Outline each Plasmodium ovale-infected red blood cell.
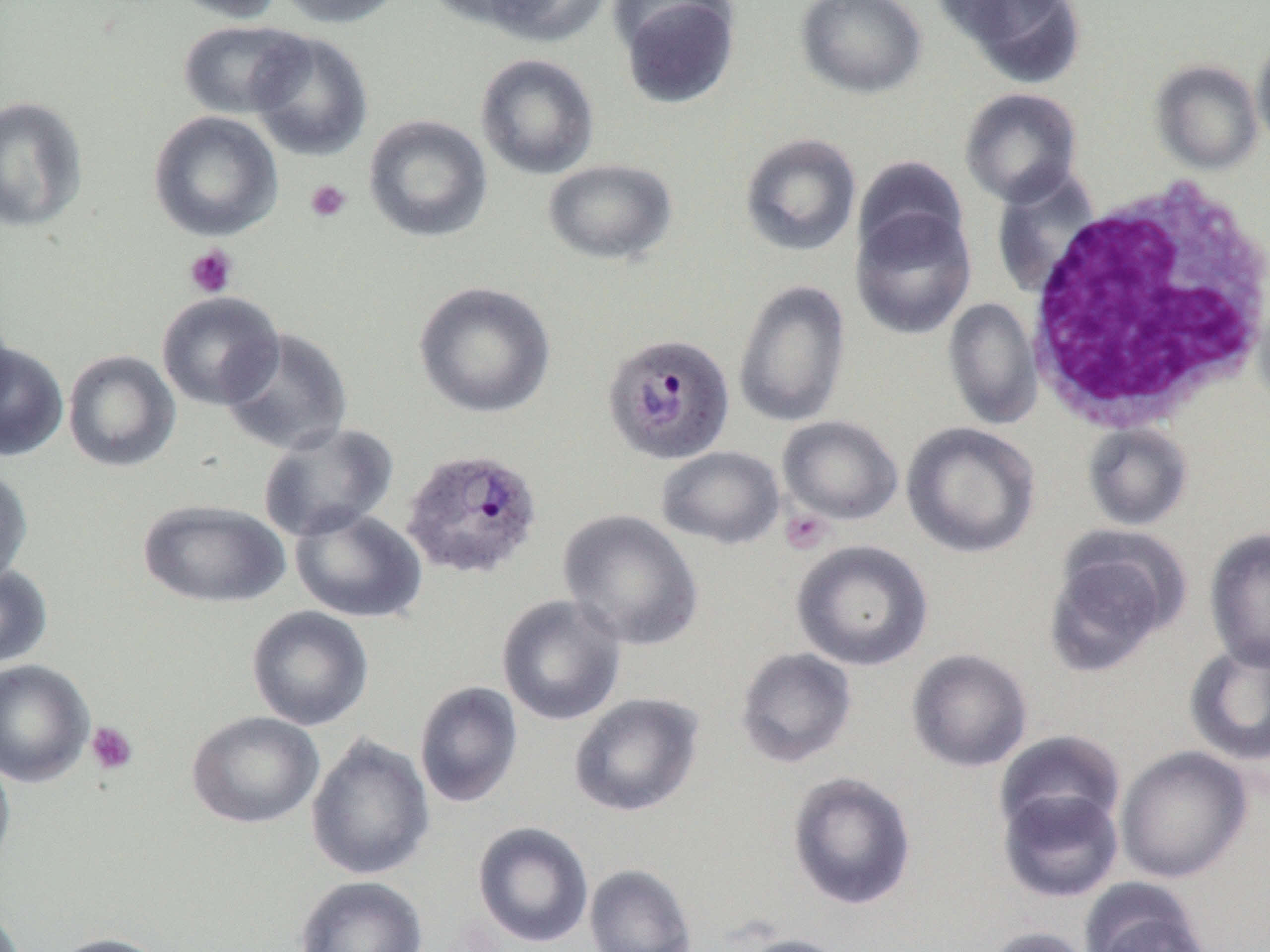
Approximate bounding boxes as (x1,y1)-(x2,y2) corner pairs in pixels.
Plasmodium ovale-infected red blood cells: (601,333)-(735,465), (401,447)-(543,581).

slide_level_diagnosis: Plasmodium ovale
magnification: 1000x
preparation: thin blood smear
field_of_view: one of a larger specimen
image_size: 1270×952 pixels
modality: light microscopy
uninfected_red_blood_cell_locations: 'approximate bounding boxes as (x1,y1)-(x2,y2) corner pairs in pixels: (165,0)-(284,23), (275,0)-(407,28), (421,0)-(556,32), (478,0)-(612,47), (611,0)-(741,109), (795,0)-(926,99), (929,0)-(1067,47), (946,0)-(1084,87), (178,19)-(310,120), (247,31)-(374,161), (1251,38)-(1270,150), (474,53)-(600,180), (1150,59)-(1263,174), (959,87)-(1083,208), (0,95)-(88,232), (148,110)-(283,242), (363,114)-(493,243), (739,132)-(862,257), (852,155)-(969,264), (542,158)-(678,266), (990,166)-(1102,299), (850,205)-(976,340), (1252,267)-(1270,411), (733,278)-(852,428), (413,281)-(556,419), (156,291)-(285,410), (942,297)-(1043,430), (0,302)-(16,420), (220,327)-(353,457), (0,341)-(69,461), (62,349)-(181,472), (777,415)-(903,525), (900,421)-(1041,558), (257,422)-(398,542), (1082,423)-(1193,531), (655,445)-(785,550), (0,467)-(33,589), (137,498)-(290,608), (289,506)-(428,624), (557,509)-(704,651), (1204,527)-(1270,672), (1043,532)-(1186,676), (791,539)-(933,671), (0,564)-(53,669), (496,594)-(627,726), (246,605)-(374,731), (1184,640)-(1270,766), (735,647)-(858,768), (906,648)-(1033,773), (0,659)-(94,788), (414,681)-(523,808), (569,692)-(704,817), (186,711)-(324,829), (994,729)-(1126,839), (305,734)-(435,881), (1115,745)-(1252,883), (0,749)-(15,881), (786,771)-(917,911), (997,786)-(1124,903), (472,821)-(594,948), (584,863)-(697,952), (294,875)-(428,952), (1079,880)-(1212,952), (0,900)-(26,952), (978,926)-(1097,952), (49,932)-(173,952), (730,933)-(854,952)'
white_blood_cell_locations: 'approximate bounding boxes as (x1,y1)-(x2,y2) corner pairs in pixels: (1021,177)-(1270,434)'
platelet_locations: 'approximate bounding boxes as (x1,y1)-(x2,y2) corner pairs in pixels: (305,179)-(352,223), (184,244)-(238,298), (779,509)-(832,555), (86,721)-(138,775)'